Outline each blood parasite and name the species.
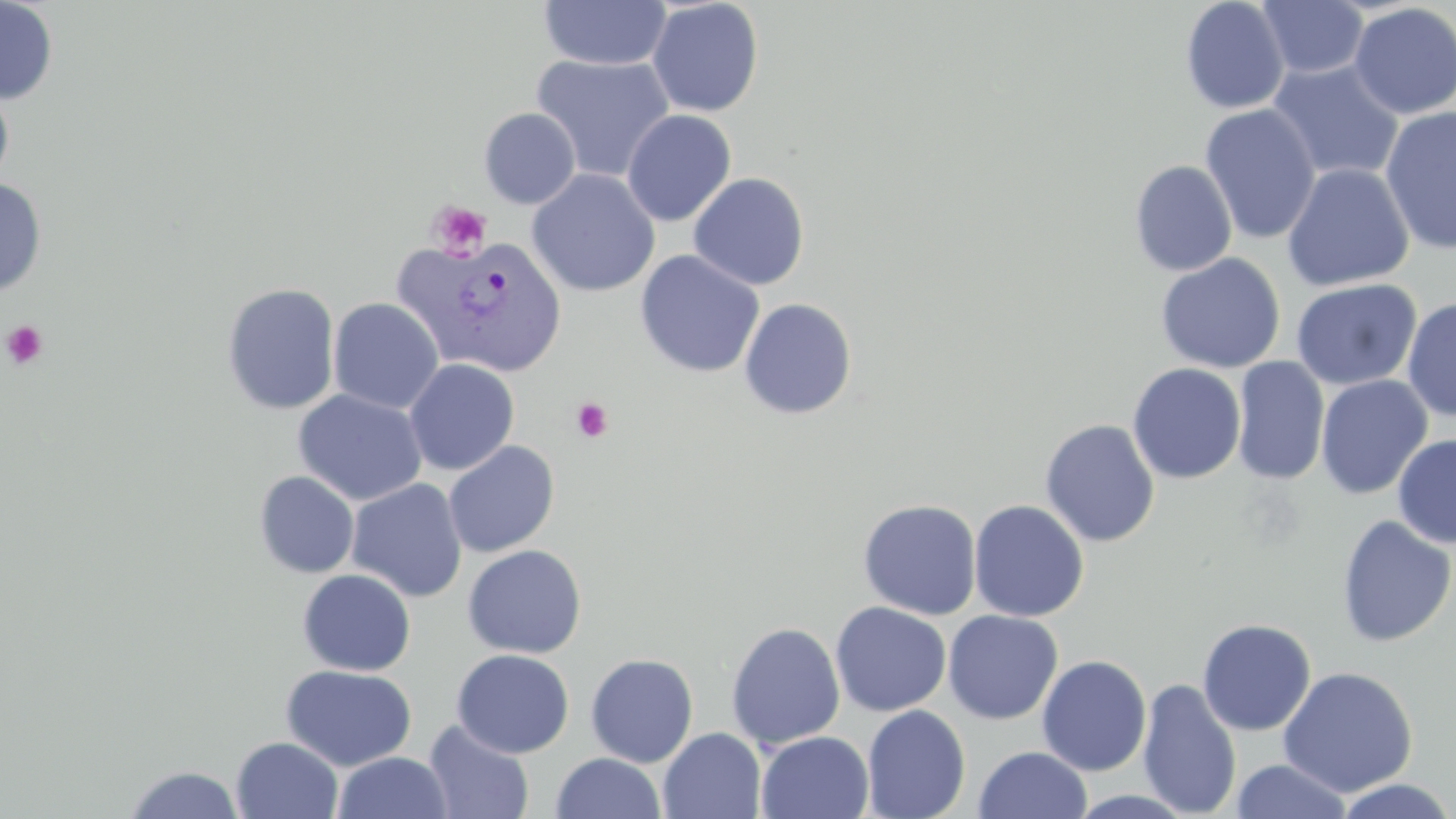

Approximate bounding boxes as [x1, y1, x2, y2] in pixels.
Plasmodium vivax-infected red blood cells: [403, 235, 569, 379].
No Plasmodium falciparum, Plasmodium ovale, Plasmodium malariae, Babesia divergens, or Trypanosoma brucei observed.

slide_level_diagnosis: Plasmodium vivax
platelet_locations: 'approximate bounding boxes as [x1, y1, x2, y2] in pixels: [427, 200, 493, 261], [2, 320, 49, 370], [571, 398, 614, 443]'
preparation: thin blood smear
magnification: 1000x
field_of_view: single
modality: light microscopy
uninfected_red_blood_cell_locations: 'approximate bounding boxes as [x1, y1, x2, y2] in pixels: [0, 0, 58, 105], [1180, 0, 1290, 115], [537, 1, 673, 70], [646, 1, 764, 117], [1256, 1, 1369, 80], [1349, 2, 1456, 119], [531, 54, 676, 183], [1267, 59, 1404, 183], [0, 82, 15, 192], [1199, 104, 1321, 245], [1380, 105, 1456, 255], [478, 107, 581, 209], [622, 110, 736, 227], [1129, 160, 1237, 277], [1282, 163, 1414, 291], [526, 169, 661, 298], [688, 172, 810, 290], [0, 178, 47, 296], [635, 250, 765, 378], [1155, 253, 1285, 373], [1290, 278, 1421, 391], [221, 283, 341, 415], [328, 297, 444, 414], [739, 297, 858, 420], [1402, 297, 1456, 421], [1231, 357, 1331, 485], [403, 358, 520, 475], [1127, 363, 1246, 484], [1315, 374, 1433, 500], [293, 389, 428, 506], [1040, 418, 1160, 547], [1393, 434, 1456, 549], [443, 440, 560, 558], [254, 471, 359, 579], [346, 478, 468, 603], [857, 498, 982, 620], [969, 499, 1090, 622], [1336, 514, 1455, 647], [462, 544, 587, 659], [297, 569, 416, 676], [830, 601, 951, 717], [943, 609, 1063, 724], [1197, 618, 1316, 736], [726, 622, 845, 749], [451, 648, 574, 758], [585, 653, 699, 767], [1036, 654, 1152, 776], [280, 663, 416, 771], [1277, 666, 1418, 798], [1137, 677, 1242, 818], [861, 705, 970, 818], [423, 719, 534, 819], [658, 727, 767, 819], [755, 731, 874, 818], [231, 736, 344, 819], [974, 746, 1092, 819], [331, 751, 454, 818], [550, 752, 666, 819], [1230, 759, 1352, 818], [121, 764, 246, 818], [1333, 777, 1456, 819], [1066, 789, 1199, 818]'
image_size: 1456×819 pixels
stain: May-Grünwald-Giemsa